Classify this cell by malaria status.
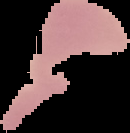

It is uninfected.

preparation = thin blood film
image size = 130×133 pixels
image type = cell region segmented out of the field of view; surrounding area masked to black